Locate every Plasmodium malariae-infected red blood cell.
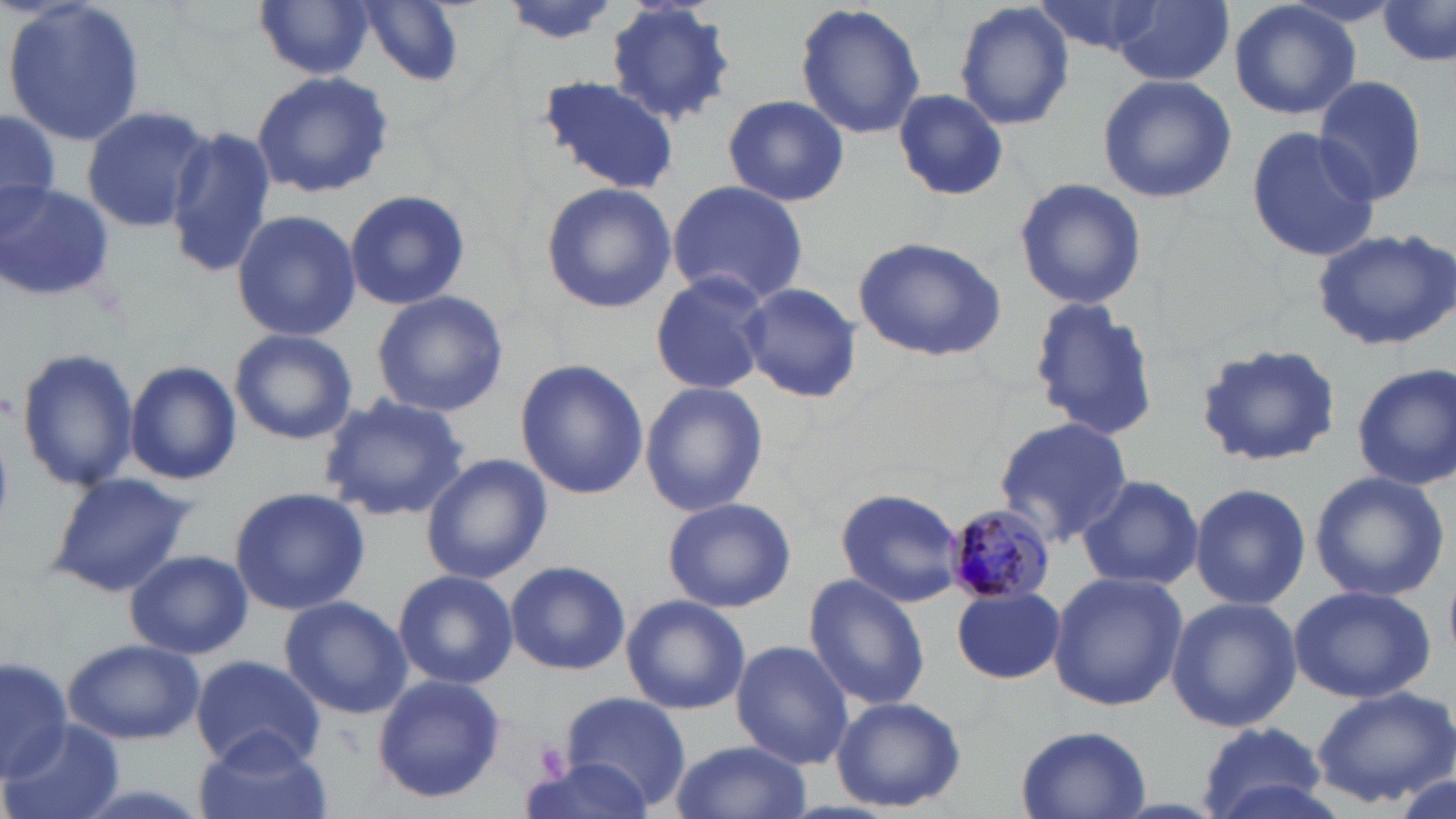
Approximate bounding boxes as named x1/y1/x2/y2 corners in pixels.
Plasmodium malariae-infected red blood cells: (x1=943, y1=504, x2=1057, y2=606).

slide-level diagnosis = Plasmodium malariae
field of view = single
magnification = 1000x
uninfected red blood cell locations = approximate bounding boxes as named x1/y1/x2/y2 corners in pixels: (x1=2, y1=0, x2=150, y2=148), (x1=358, y1=0, x2=466, y2=86), (x1=499, y1=0, x2=617, y2=47), (x1=952, y1=0, x2=1074, y2=131), (x1=1110, y1=0, x2=1234, y2=86), (x1=1228, y1=0, x2=1362, y2=121), (x1=255, y1=1, x2=374, y2=82), (x1=604, y1=1, x2=736, y2=128), (x1=1031, y1=1, x2=1171, y2=57), (x1=795, y1=2, x2=926, y2=141), (x1=1379, y1=3, x2=1455, y2=70), (x1=250, y1=68, x2=394, y2=198), (x1=539, y1=73, x2=677, y2=194), (x1=1097, y1=74, x2=1236, y2=204), (x1=1312, y1=75, x2=1429, y2=209), (x1=892, y1=88, x2=1009, y2=202), (x1=724, y1=95, x2=847, y2=206), (x1=80, y1=103, x2=212, y2=232), (x1=1, y1=107, x2=60, y2=216), (x1=1245, y1=124, x2=1383, y2=264), (x1=166, y1=125, x2=279, y2=279), (x1=1013, y1=176, x2=1146, y2=311), (x1=667, y1=180, x2=809, y2=307), (x1=0, y1=181, x2=117, y2=305), (x1=540, y1=182, x2=672, y2=313), (x1=343, y1=191, x2=470, y2=311), (x1=230, y1=209, x2=362, y2=342), (x1=1313, y1=228, x2=1456, y2=351), (x1=852, y1=236, x2=1008, y2=362), (x1=650, y1=271, x2=772, y2=394), (x1=738, y1=282, x2=863, y2=403), (x1=370, y1=290, x2=510, y2=417), (x1=1027, y1=301, x2=1162, y2=440), (x1=229, y1=328, x2=358, y2=445), (x1=1194, y1=342, x2=1344, y2=469), (x1=17, y1=347, x2=140, y2=490), (x1=515, y1=359, x2=649, y2=499), (x1=124, y1=360, x2=242, y2=486), (x1=1353, y1=363, x2=1456, y2=491), (x1=643, y1=383, x2=767, y2=518), (x1=318, y1=391, x2=471, y2=521), (x1=993, y1=415, x2=1135, y2=544), (x1=422, y1=454, x2=552, y2=584), (x1=1307, y1=469, x2=1450, y2=604), (x1=46, y1=472, x2=197, y2=598), (x1=1075, y1=474, x2=1203, y2=590), (x1=1189, y1=482, x2=1310, y2=610), (x1=229, y1=487, x2=371, y2=614), (x1=836, y1=487, x2=964, y2=607), (x1=662, y1=498, x2=796, y2=613), (x1=124, y1=550, x2=253, y2=659), (x1=504, y1=563, x2=630, y2=676), (x1=393, y1=570, x2=517, y2=688), (x1=1048, y1=570, x2=1186, y2=712), (x1=804, y1=574, x2=929, y2=711), (x1=1288, y1=584, x2=1436, y2=704), (x1=953, y1=586, x2=1066, y2=684), (x1=622, y1=594, x2=748, y2=715), (x1=279, y1=596, x2=413, y2=720), (x1=1166, y1=597, x2=1304, y2=732), (x1=60, y1=638, x2=207, y2=744), (x1=730, y1=640, x2=853, y2=768), (x1=191, y1=655, x2=328, y2=770), (x1=1, y1=656, x2=70, y2=779), (x1=371, y1=675, x2=506, y2=803), (x1=1311, y1=686, x2=1455, y2=808), (x1=561, y1=692, x2=691, y2=812), (x1=832, y1=696, x2=965, y2=812), (x1=0, y1=720, x2=126, y2=819), (x1=1193, y1=720, x2=1329, y2=816), (x1=1015, y1=725, x2=1153, y2=819), (x1=194, y1=729, x2=330, y2=819), (x1=670, y1=738, x2=811, y2=819), (x1=519, y1=757, x2=658, y2=819), (x1=1395, y1=770, x2=1453, y2=819)
modality = optical microscopy
image size = 1456×819 pixels
preparation = thin blood smear
platelet locations = approximate bounding boxes as named x1/y1/x2/y2 corners in pixels: (x1=533, y1=737, x2=573, y2=783)
stain = May-Grünwald-Giemsa